Name the parasite shown.
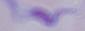
This is a trypanosome.

Photomicrograph. 1000x magnification.